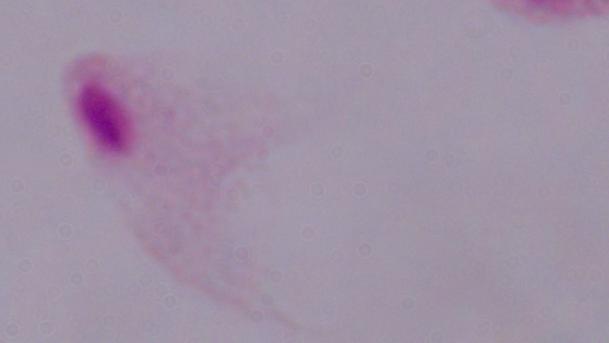

A trichomonad is shown. Captured at 1000x magnification. Photomicrograph.